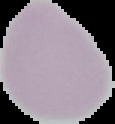 The area outside the segmented cell region is set to black. Image is 115×124 pixels. From a thin blood smear. Result: no malaria parasites detected.